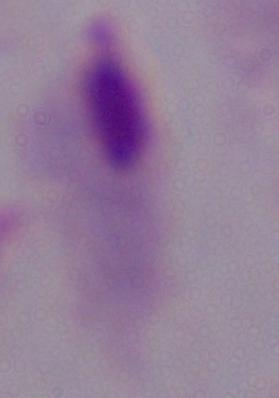
A trichomonad is shown. 1000x magnification. Photomicrograph.